Outline platelets.
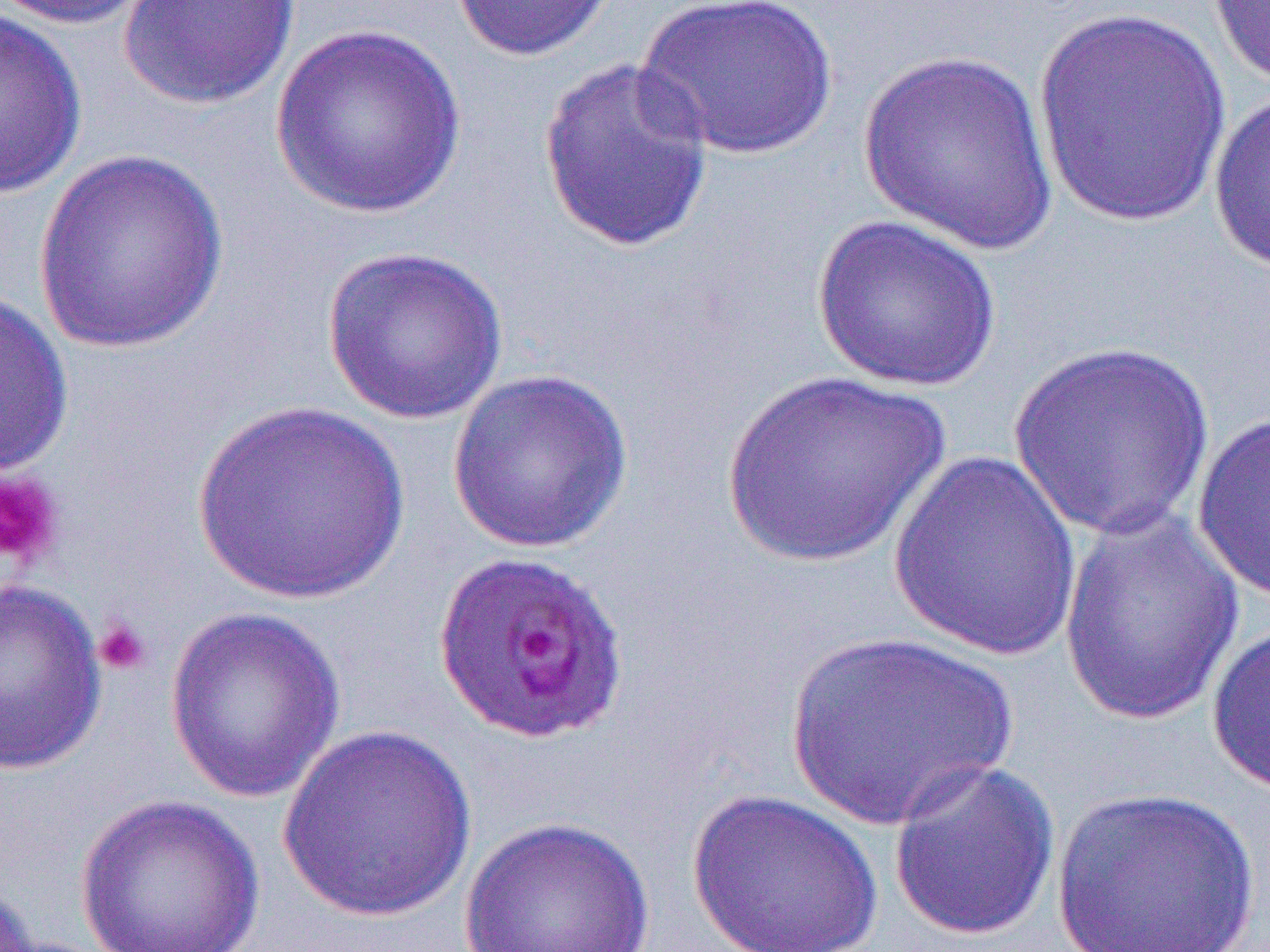

Approximate bounding boxes as [x1, y1, x2, y2] in pixels.
Platelets: [0, 469, 65, 570], [92, 617, 153, 677].

Summary:
  - Uninfected red blood cell locations: [3, 0, 161, 29], [119, 0, 302, 110], [448, 0, 619, 62], [633, 0, 842, 161], [1206, 0, 1270, 88], [1029, 6, 1230, 227], [0, 8, 87, 198], [269, 23, 468, 219], [857, 49, 1062, 254], [536, 56, 715, 254], [1208, 87, 1270, 275], [32, 148, 230, 355], [810, 213, 1004, 392], [321, 245, 510, 424], [0, 290, 73, 479], [1007, 340, 1217, 541], [446, 366, 634, 553], [721, 370, 950, 569], [190, 401, 411, 605], [1192, 409, 1270, 606], [887, 448, 1084, 661], [1056, 505, 1247, 728], [0, 578, 109, 776], [164, 606, 346, 804], [1206, 621, 1270, 797], [785, 629, 1019, 829], [276, 724, 478, 924], [887, 758, 1061, 941], [1050, 785, 1262, 950], [683, 786, 887, 952], [72, 792, 267, 952], [458, 815, 657, 952]
  - Slide-level diagnosis: Plasmodium falciparum
  - Magnification: 1000x
  - Field of view: one of a larger specimen
  - Image size: 1270×952 pixels
  - Modality: optical microscopy
  - Preparation: thin blood smear